Identify the parasite.
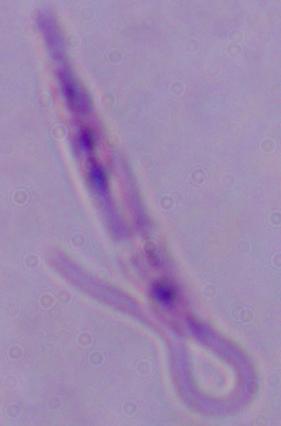

Leishmania.

modality = micrograph
magnification = 1000x